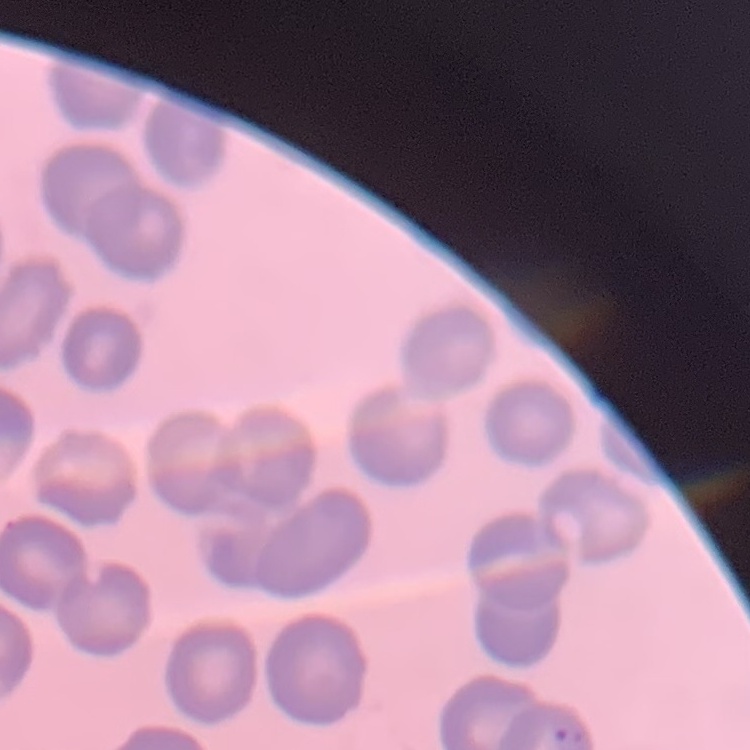
The erythrocytes exhibit no rouleaux formation. Thin peripheral smear. One tile cut from a larger photomicrograph. Field's or Giemsa stain.